Locate every blood parasite and identify its species.
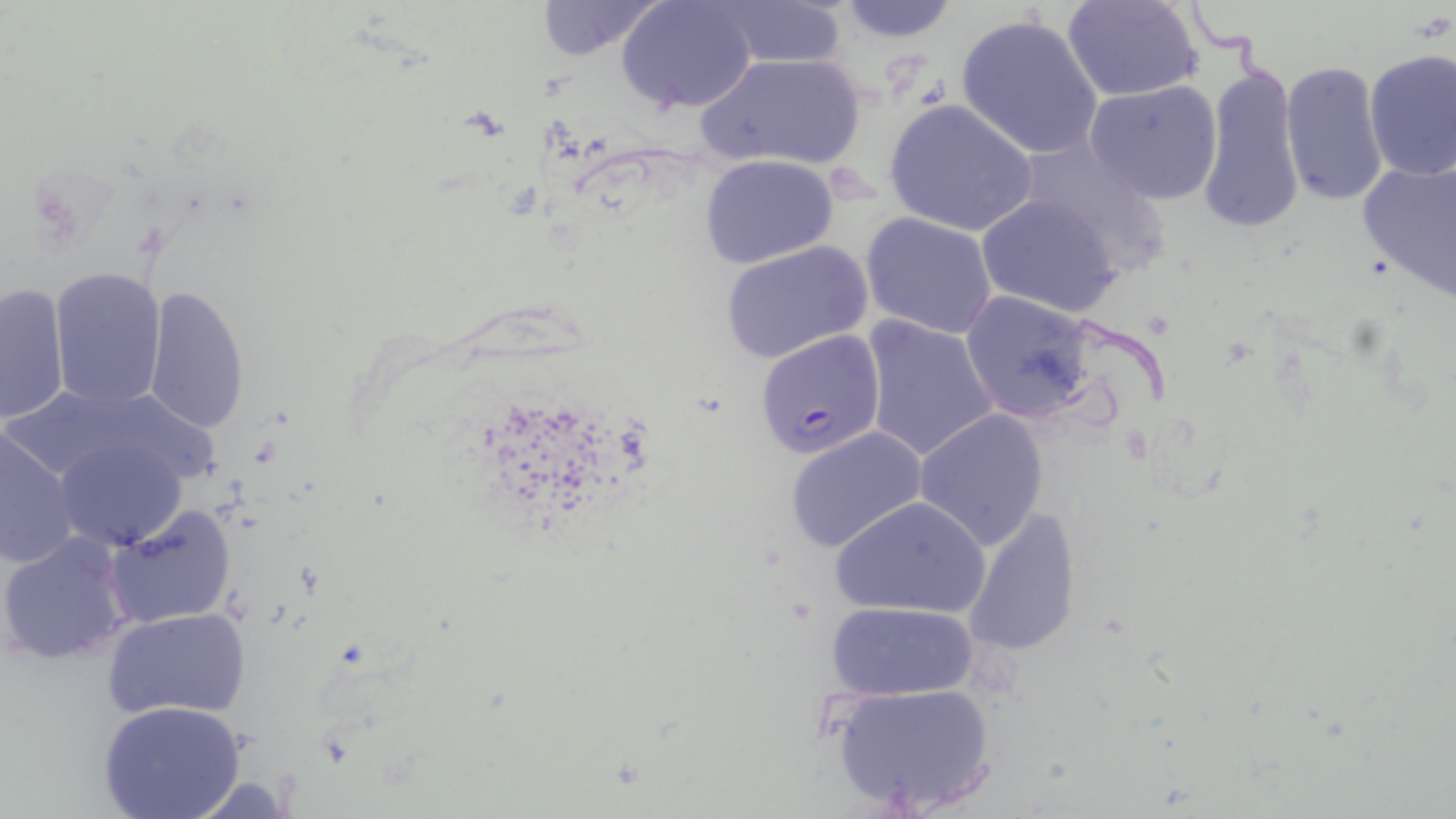
Approximate bounding boxes as [x1, y1, x2, y2] in pixels.
Plasmodium falciparum-infected red blood cells: [760, 330, 894, 458].
No Plasmodium ovale, Plasmodium malariae, Plasmodium vivax, Babesia divergens, or Trypanosoma brucei observed.

Summary:
  - Uninfected red blood cell locations: [533, 0, 667, 60], [618, 0, 758, 115], [828, 0, 961, 43], [711, 1, 852, 68], [1062, 1, 1207, 102], [953, 14, 1104, 160], [1362, 49, 1456, 181], [695, 52, 869, 172], [1280, 61, 1390, 207], [1197, 62, 1305, 235], [1084, 80, 1224, 204], [883, 98, 1039, 237], [1010, 137, 1174, 277], [698, 154, 840, 269], [1356, 157, 1456, 301], [975, 192, 1125, 317], [860, 211, 999, 339], [717, 239, 873, 367], [47, 264, 168, 408], [1, 281, 71, 424], [142, 286, 250, 438], [959, 290, 1096, 423], [861, 313, 1000, 464], [913, 409, 1049, 549], [0, 425, 81, 570], [784, 425, 930, 555], [54, 437, 189, 551], [832, 494, 993, 619], [105, 504, 238, 629], [962, 505, 1081, 659], [2, 530, 134, 667], [826, 600, 979, 702], [101, 607, 251, 720], [828, 680, 998, 813], [99, 700, 247, 819]
  - Slide-level diagnosis: Plasmodium falciparum
  - Stain: May-Grünwald-Giemsa
  - Magnification: 1000x
  - Field of view: single
  - Modality: optical microscopy
  - Image size: 1456×819 pixels
  - Preparation: thin blood film